Find the red blood cells that are infected with P. falciparum, and any of indeterminate infection status.
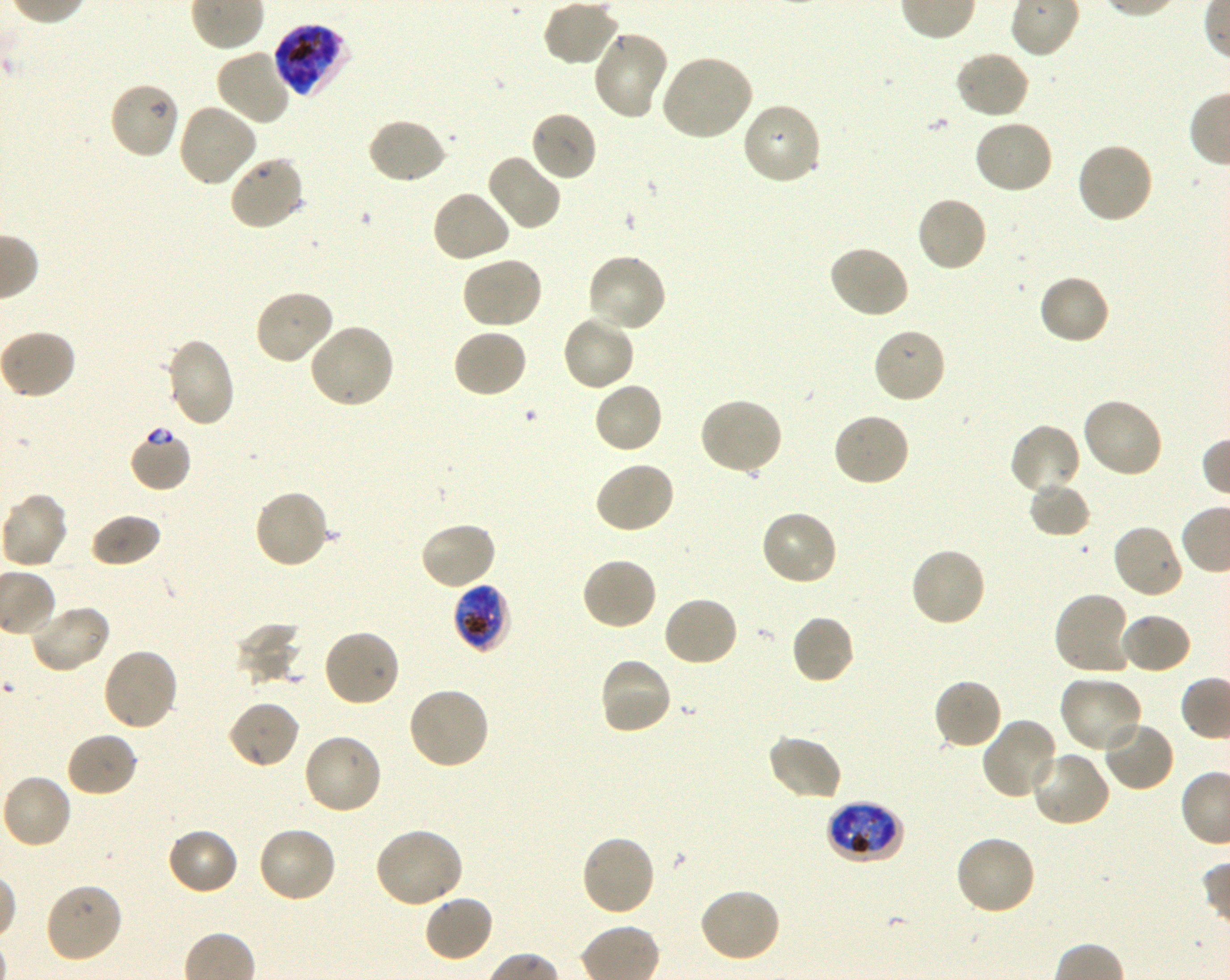

Approximate bounding boxes as (x1, y1, x2, y2) in pixels. Not every red blood cell is marked. A life-cycle stage — or a range of stages, where the recorded stages span more than one — follows each staged infected red blood cell.
Infected red blood cells: (273, 22, 352, 98) late trophozoite to late schizont; (452, 584, 511, 654) late trophozoite to early schizont; (826, 801, 905, 865) early trophozoite to late schizont.
Red blood cells of indeterminate infection status: (129, 429, 193, 492).

Locations of uninfected red blood cells: (543, 0, 620, 68), (591, 30, 669, 120), (215, 47, 292, 127), (954, 49, 1031, 119), (659, 54, 754, 142), (109, 80, 180, 160), (177, 101, 258, 188), (741, 101, 823, 186), (529, 110, 598, 182), (365, 117, 448, 186), (973, 118, 1055, 195), (1074, 141, 1154, 224), (485, 152, 563, 232), (228, 154, 306, 232), (430, 189, 512, 265), (915, 195, 989, 275), (826, 244, 910, 319), (585, 253, 668, 334), (461, 255, 544, 330), (1037, 273, 1111, 346), (253, 289, 336, 366), (560, 313, 636, 393), (308, 323, 396, 410), (872, 326, 947, 405), (451, 328, 529, 399), (0, 329, 77, 400), (164, 337, 237, 428), (592, 380, 664, 454), (697, 396, 784, 476), (1081, 396, 1164, 479), (832, 412, 911, 488), (1009, 422, 1081, 497), (593, 460, 675, 535), (1028, 482, 1091, 538), (252, 489, 330, 570), (0, 491, 69, 570), (758, 509, 839, 587), (88, 513, 163, 568), (419, 520, 497, 591), (1112, 524, 1185, 600), (910, 546, 986, 629), (581, 556, 659, 631), (1053, 590, 1134, 677), (662, 595, 740, 668), (26, 604, 111, 674), (1117, 612, 1193, 676), (790, 614, 855, 686), (234, 623, 304, 687), (322, 629, 401, 709), (101, 647, 180, 732), (597, 655, 673, 735), (1059, 676, 1143, 755), (933, 677, 1003, 751), (406, 686, 490, 771), (226, 700, 300, 769), (980, 717, 1060, 802), (1101, 718, 1176, 792), (65, 731, 139, 798), (302, 732, 383, 816), (766, 733, 843, 803), (1028, 749, 1112, 828), (0, 773, 73, 850), (256, 826, 338, 904), (373, 826, 465, 909), (166, 827, 240, 896), (580, 834, 657, 917), (953, 834, 1037, 917), (42, 883, 123, 965), (698, 886, 783, 963), (422, 893, 494, 963). Oil immersion, 100x objective (numerical aperture 1.30). Blood group of the donor: O+. P. falciparum strain 3D7 in shaking in-vitro culture. Giemsa stain. Image is 1230×980 pixels. Thin blood smear. One field from this slide.